Locate every Plasmodium parasite.
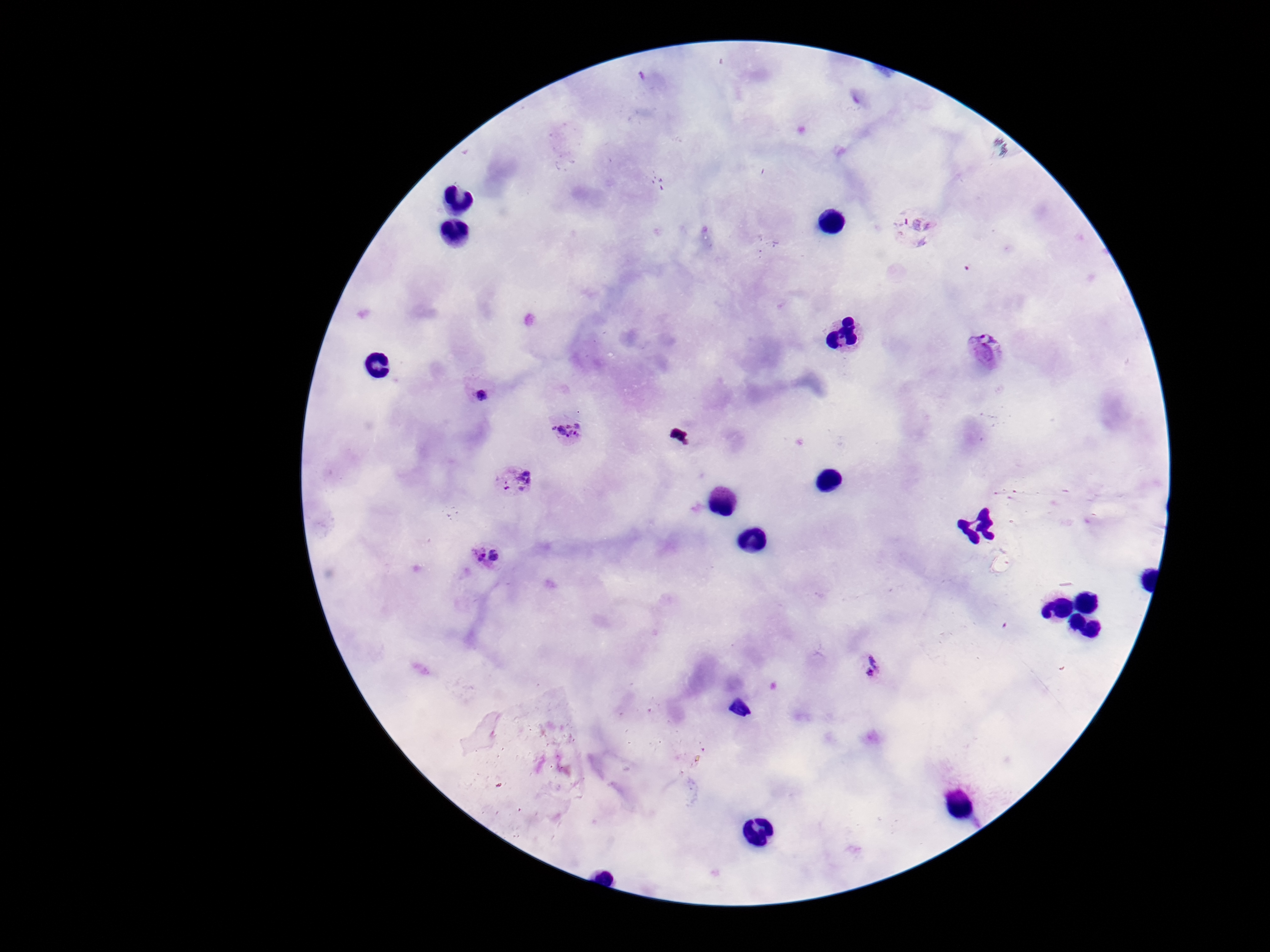
Approximate centers as [x, y] in pixels.
Plasmodium parasites: [912, 227], [987, 350], [478, 391], [570, 430], [514, 482], [486, 558], [873, 666].

Summary:
  - Magnification: 100x
  - Preparation: thick peripheral-blood smear
  - Patient malaria status: infected
  - Stain: Giemsa
  - Field of view: single
  - Capture: smartphone camera through the microscope eyepiece
  - Image size: 1270×952 pixels